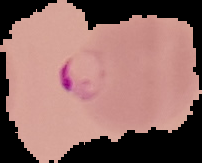

Summary:
  - Image type: cell region segmented out of the field of view; surrounding area masked to black
  - Image size: 202×163 pixels
  - Result: Plasmodium parasites identified
  - Preparation: thin blood film